Identify the parasite.
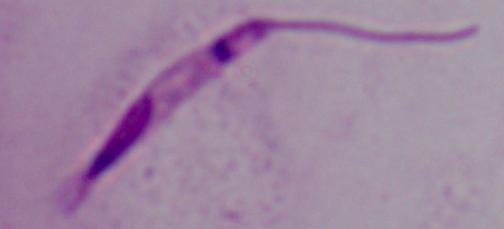

Leishmania.

Summary:
  - Magnification: 1000x
  - Modality: micrograph